Assess the morphology of the erythrocytes.
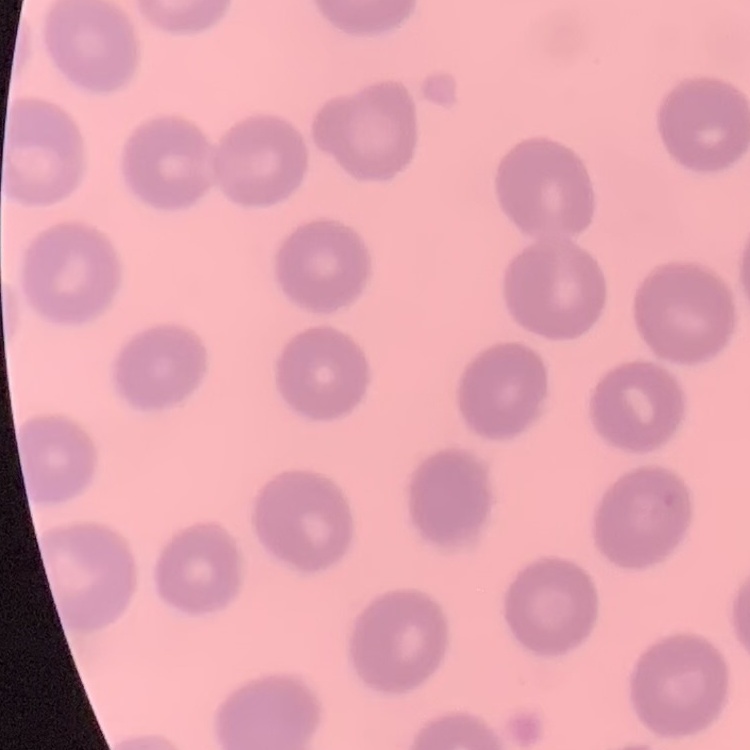

No rouleaux formation.

stain = Field's or Giemsa
image type = one tile cut from a larger photomicrograph
preparation = thin blood smear